Identify the parasite.
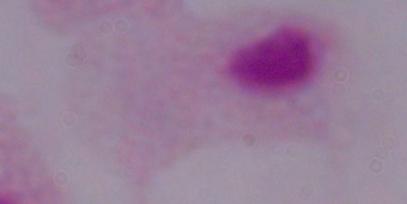

This is a trichomonad.

modality: micrograph
magnification: 1000x